Name the parasite shown.
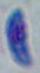
This is Toxoplasma gondii.

modality = micrograph
magnification = 1000x